Report the malaria status of this cell.
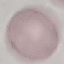

It is uninfected.

Summary:
  - Image type: automatically extracted cell patch, resized to 64 × 64 pixels
  - Stain: Giemsa
  - Capture: smartphone camera at the microscope eyepiece
  - Preparation: thin blood film